Point out each Plasmodium parasite.
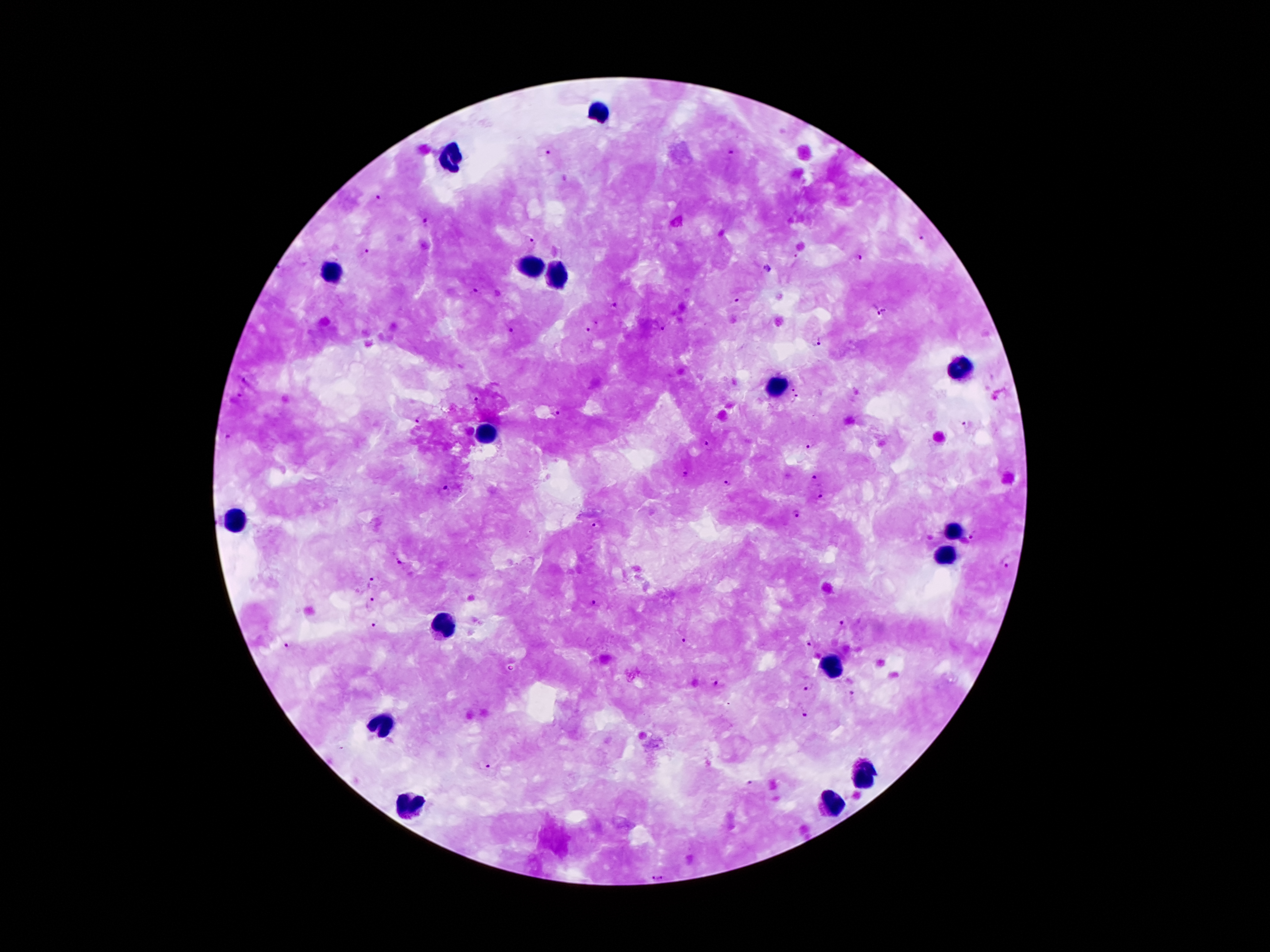

Approximate centers as [x, y] in pixels.
Plasmodium parasites: [548, 151], [730, 152], [380, 200], [427, 222], [922, 238], [531, 240], [369, 249], [859, 257], [767, 269], [478, 291], [735, 299], [614, 304], [888, 308], [870, 312], [588, 328], [661, 328], [511, 330], [819, 341], [245, 380], [793, 388], [797, 397], [239, 398], [475, 398], [557, 412], [417, 421], [967, 425], [231, 439], [706, 443], [813, 445], [687, 476], [814, 477], [727, 485], [445, 491], [821, 492], [795, 514], [597, 527], [972, 534], [1006, 563], [402, 564], [373, 582], [370, 601], [592, 603], [844, 622], [374, 625], [685, 642], [812, 644], [289, 646], [714, 682], [809, 686], [852, 695], [807, 712], [487, 766], [751, 786], [664, 876], [650, 879].

Summary:
  - Leukocyte locations: [604, 110], [451, 159], [528, 269], [332, 272], [553, 278], [959, 371], [776, 387], [484, 435], [232, 521], [953, 530], [944, 559], [438, 625], [831, 669], [380, 727], [867, 771], [831, 804], [411, 806]
  - Patient malaria status: positive for Plasmodium falciparum
  - Magnification: 100x
  - Preparation: thick peripheral-blood smear
  - Image size: 1270×952 pixels
  - Stain: Giemsa
  - Field of view: single
  - Capture: smartphone through the microscope eyepiece